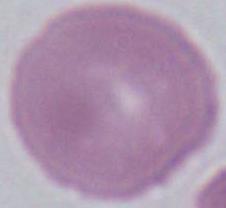

An erythrocyte is seen. Photomicrograph. Captured at 1000x magnification.